Describe the morphology of the erythrocytes.
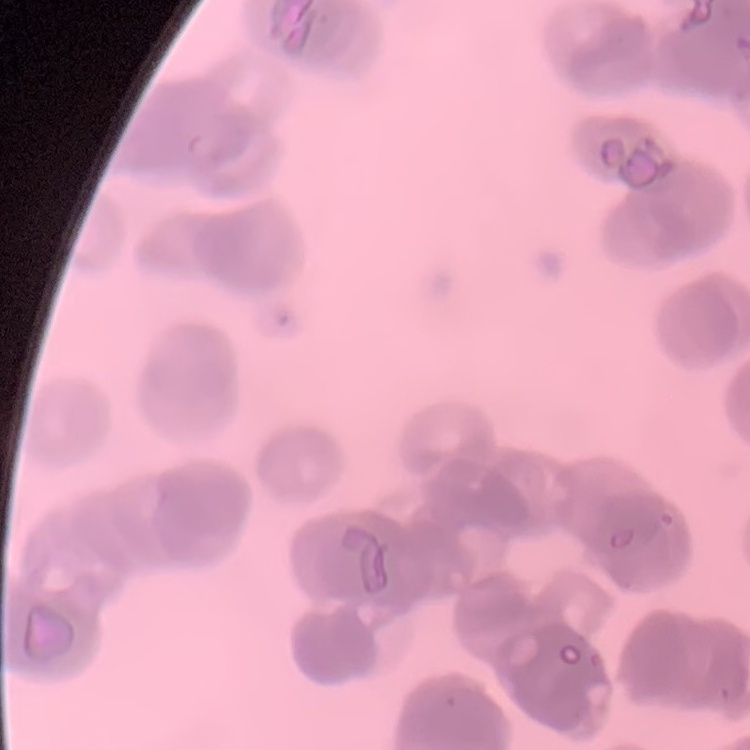

Rouleaux formation.

image type = square crop of a larger photomicrograph
preparation = thin blood film
stain = Field's or Giemsa